Identify the cell.
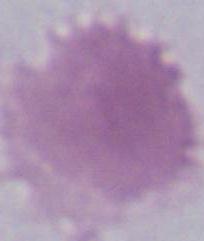
An erythrocyte.

magnification = 1000x
modality = micrograph